Outline each blood parasite and name the species.
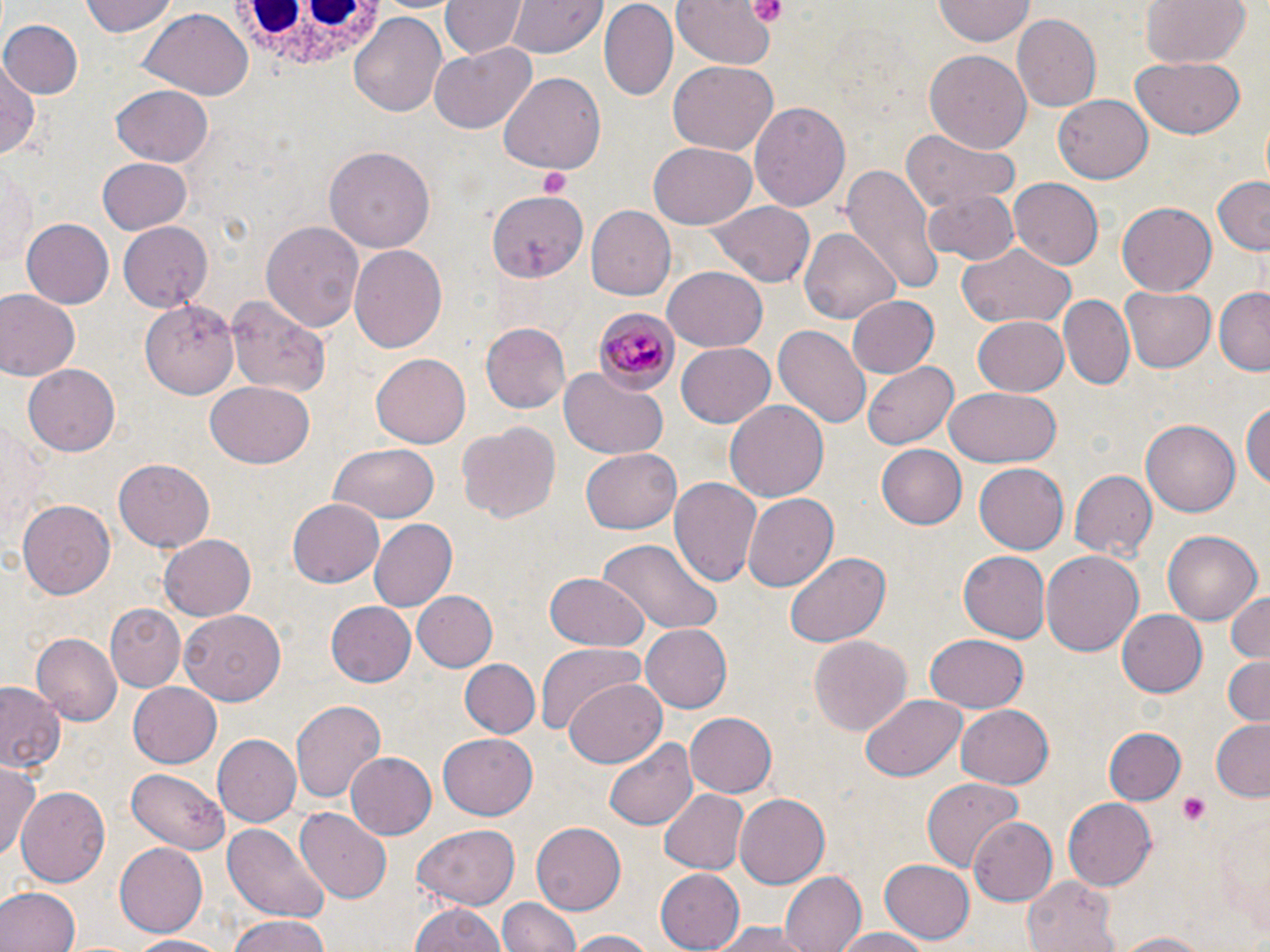

Approximate bounding boxes as [x1, y1, x2, y2] in pixels.
Plasmodium malariae-infected red blood cells: [597, 308, 682, 390].
No Plasmodium falciparum, Plasmodium ovale, Plasmodium vivax, Babesia divergens, or Trypanosoma brucei observed.

Uninfected red blood cell locations: [79, 0, 178, 38], [442, 0, 525, 59], [512, 0, 604, 59], [668, 0, 778, 72], [1140, 0, 1252, 70], [601, 1, 678, 102], [932, 2, 1035, 45], [139, 9, 254, 99], [1011, 13, 1100, 112], [348, 14, 448, 117], [2, 17, 83, 99], [430, 43, 538, 133], [924, 49, 1033, 154], [1131, 57, 1247, 139], [0, 58, 42, 161], [667, 63, 777, 154], [497, 73, 606, 174], [109, 84, 214, 169], [1055, 95, 1152, 183], [750, 101, 851, 215], [901, 132, 1019, 215], [647, 142, 757, 229], [324, 146, 434, 253], [97, 156, 192, 234], [1, 158, 38, 270], [844, 162, 944, 296], [1211, 174, 1270, 255], [1008, 179, 1102, 270], [487, 189, 586, 281], [922, 190, 1019, 266], [706, 200, 815, 287], [1117, 202, 1216, 296], [585, 206, 674, 301], [21, 218, 116, 309], [261, 221, 367, 334], [116, 222, 214, 310], [800, 226, 901, 323], [348, 242, 448, 354], [956, 243, 1078, 331], [662, 265, 767, 352], [1119, 285, 1215, 374], [1215, 286, 1270, 373], [0, 290, 81, 381], [848, 294, 940, 378], [225, 295, 331, 398], [1062, 295, 1134, 389], [141, 297, 241, 397], [972, 315, 1071, 396], [482, 323, 570, 416], [773, 325, 871, 431], [677, 344, 774, 427], [372, 353, 472, 447], [863, 362, 959, 450], [24, 364, 119, 457], [560, 368, 668, 461], [203, 383, 313, 469], [944, 387, 1062, 467], [1242, 396, 1270, 495], [725, 399, 831, 503], [0, 410, 46, 547], [1142, 417, 1242, 518], [456, 420, 561, 525], [329, 443, 438, 526], [877, 445, 970, 528], [581, 450, 680, 533], [113, 458, 216, 550], [975, 463, 1068, 554], [1070, 470, 1156, 559], [670, 476, 762, 589], [741, 491, 838, 592], [18, 499, 116, 601], [288, 500, 384, 587], [368, 519, 459, 612], [1163, 530, 1261, 626], [160, 533, 259, 620], [596, 539, 724, 635], [785, 551, 891, 648], [958, 551, 1050, 642], [1042, 551, 1143, 657], [544, 573, 649, 651], [1224, 589, 1270, 666], [411, 591, 497, 672], [326, 600, 417, 688], [106, 605, 186, 691], [1117, 608, 1207, 698], [179, 609, 288, 703], [643, 625, 733, 711], [32, 633, 121, 723], [809, 634, 912, 733], [925, 635, 1028, 712], [533, 638, 648, 738], [1220, 654, 1270, 727], [459, 658, 540, 740], [564, 677, 667, 768], [125, 680, 221, 768], [1, 684, 64, 771], [861, 694, 967, 781], [290, 697, 386, 804], [956, 705, 1054, 788], [683, 710, 776, 799], [1210, 721, 1269, 799], [1105, 727, 1185, 804], [438, 730, 537, 819], [215, 734, 299, 827], [605, 735, 697, 831], [347, 752, 436, 838], [0, 763, 41, 861], [128, 769, 230, 855], [923, 778, 1026, 871], [17, 786, 110, 887], [658, 787, 750, 875], [735, 795, 830, 886], [1063, 797, 1157, 888], [294, 807, 392, 903], [967, 815, 1057, 907], [531, 821, 626, 917], [221, 823, 331, 921], [412, 824, 521, 910], [112, 842, 208, 937], [879, 859, 975, 944], [657, 866, 749, 952], [776, 869, 865, 952], [1022, 874, 1120, 950], [0, 887, 78, 952], [500, 895, 578, 952], [410, 901, 507, 952], [221, 918, 336, 952], [712, 921, 813, 952], [827, 927, 936, 952], [1110, 929, 1221, 951], [564, 930, 662, 952], [130, 933, 228, 950]. White blood cell locations: [224, 3, 391, 68]. Platelet locations: [745, 0, 790, 26], [535, 165, 569, 197], [1179, 795, 1210, 824]. Slide-level diagnosis: Plasmodium malariae. Light microscopy. One field of a larger specimen. Image is 1270×952 pixels. Thin blood smear. May-Grünwald-Giemsa stain. 1000x magnification.